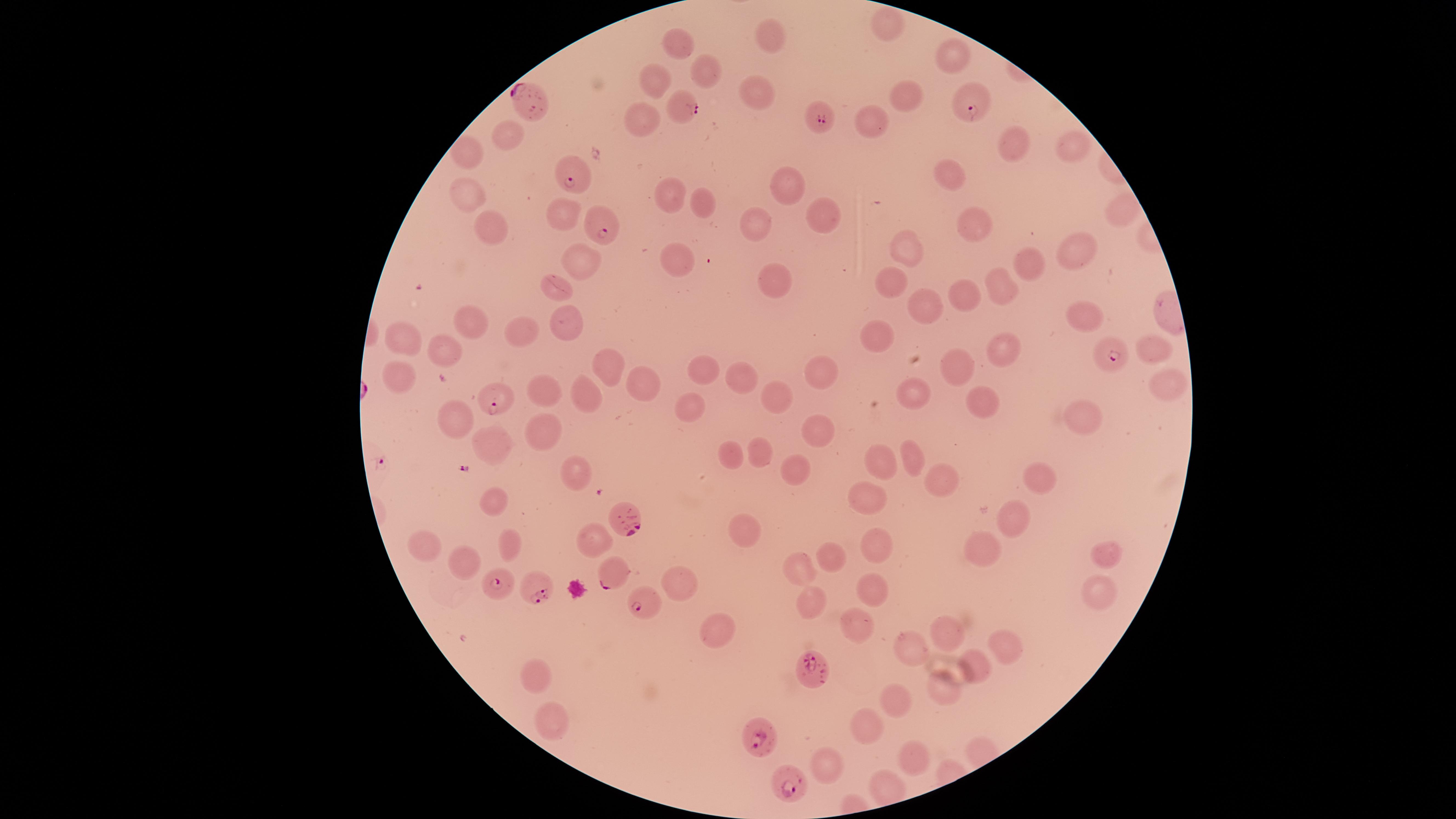

capture = smartphone photograph through the microscope eyepiece
field of view = single
presence = malaria parasites identified
parasitized red blood cells = approximate marker points as {x, y} in pixels: {968, 99}, {686, 102}, {529, 105}, {822, 119}, {572, 173}, {601, 226}, {1115, 355}, {499, 402}, {625, 515}, {610, 575}, {495, 583}, {532, 588}, {644, 605}, {810, 668}, {758, 735}, {787, 779}
visible region = circular
stain = Giemsa
image size = 1456×819 pixels
preparation = thin smear of blood
uninfected red blood cells = approximate marker points as {x, y} in pixels: {883, 25}, {769, 33}, {678, 42}, {948, 54}, {704, 70}, {654, 85}, {754, 94}, {906, 99}, {645, 119}, {868, 122}, {512, 134}, {1019, 143}, {1067, 149}, {463, 157}, {949, 177}, {790, 185}, {668, 196}, {697, 199}, {470, 203}, {1117, 207}, {823, 213}, {561, 215}, {972, 224}, {491, 229}, {757, 230}, {907, 248}, {1075, 253}, {678, 257}, {573, 261}, {1028, 266}, {776, 276}, {896, 285}, {1004, 288}, {556, 289}, {963, 299}, {925, 304}, {1087, 313}, {470, 323}, {524, 330}, {570, 331}, {879, 340}, {407, 341}, {1152, 348}, {448, 353}, {1002, 355}, {953, 363}, {609, 369}, {703, 369}, {814, 370}, {743, 371}, {401, 372}, {1164, 386}, {644, 387}, {590, 392}, {920, 392}, {545, 393}, {775, 397}, {988, 401}, {689, 408}, {454, 415}, {1083, 419}, {543, 427}, {811, 431}, {494, 448}, {758, 450}, {735, 454}, {914, 454}, {878, 462}, {795, 469}, {574, 470}, {1037, 476}, {936, 483}, {862, 495}, {491, 508}, {1017, 522}, {744, 535}, {428, 539}, {515, 545}, {874, 548}, {980, 548}, {832, 554}, {464, 558}, {1106, 558}, {803, 569}, {682, 580}, {871, 593}, {1096, 594}, {811, 600}, {718, 629}, {860, 631}, {946, 633}, {1007, 645}, {916, 646}, {973, 667}, {537, 674}, {945, 684}, {896, 699}, {551, 719}, {869, 725}, {913, 752}, {825, 759}
species = Plasmodium falciparum